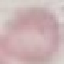 Result: no malaria parasites seen. Photographed with a smartphone camera at the microscope eyepiece. Giemsa-stained preparation. Automatically extracted cell patch, resized to 64 × 64 pixels. Thin blood smear.